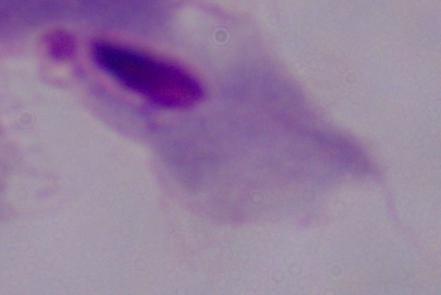 Captured at 1000x magnification. Micrograph. A trichomonad is seen.